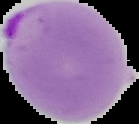

Summary:
  - Image size: 139×124 pixels
  - Image type: segmented cell region on a black background
  - Malaria status: parasitized
  - Preparation: thin blood film